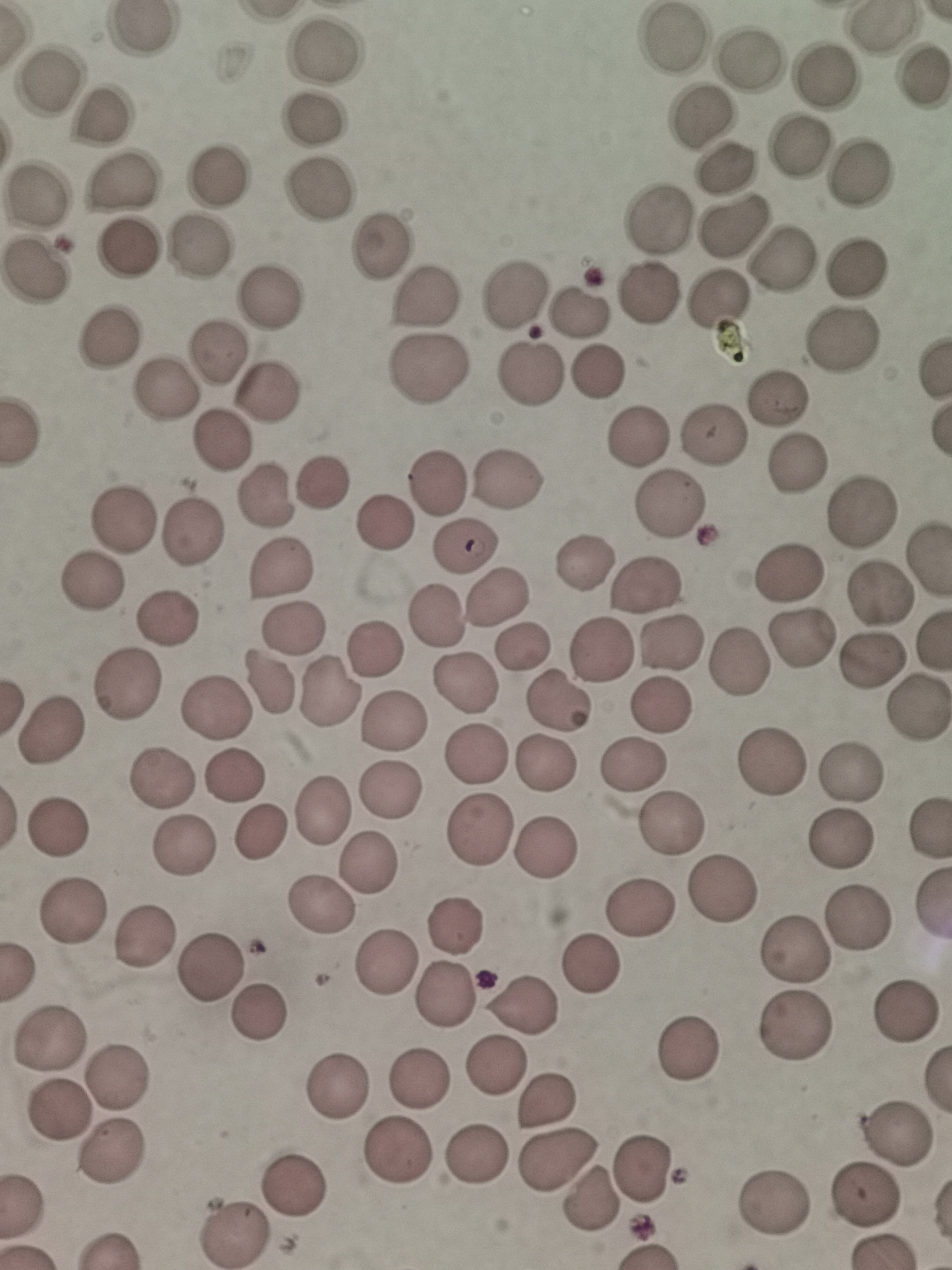

Approximate object centers, in pixels from the top-left corner.
Summary:
  - Cell locations: (x=671, y=41), (x=324, y=52), (x=752, y=59), (x=825, y=76), (x=918, y=76), (x=48, y=82), (x=99, y=114), (x=701, y=117), (x=313, y=123), (x=797, y=144), (x=727, y=167), (x=857, y=171), (x=216, y=174), (x=124, y=182), (x=319, y=194), (x=37, y=195), (x=655, y=220), (x=731, y=225), (x=380, y=246), (x=130, y=247), (x=200, y=248), (x=781, y=258), (x=856, y=267), (x=38, y=269), (x=517, y=294), (x=648, y=294), (x=423, y=296), (x=268, y=299), (x=721, y=301), (x=578, y=312), (x=108, y=336), (x=844, y=342), (x=217, y=352), (x=423, y=369), (x=597, y=372), (x=530, y=374), (x=166, y=391), (x=268, y=393), (x=776, y=400), (x=715, y=434), (x=638, y=437), (x=219, y=441), (x=797, y=463), (x=509, y=479), (x=438, y=481), (x=323, y=482), (x=266, y=497), (x=671, y=505), (x=862, y=510), (x=124, y=520), (x=387, y=521), (x=194, y=531), (x=466, y=546), (x=584, y=561), (x=277, y=568), (x=790, y=572), (x=90, y=582), (x=649, y=588), (x=496, y=594), (x=879, y=594), (x=432, y=617), (x=168, y=618), (x=294, y=630), (x=800, y=638), (x=670, y=640), (x=523, y=646), (x=375, y=649), (x=604, y=649), (x=872, y=657), (x=739, y=660), (x=269, y=683), (x=127, y=684), (x=462, y=684), (x=330, y=695), (x=556, y=700), (x=663, y=704), (x=915, y=706), (x=215, y=711), (x=392, y=720), (x=50, y=729), (x=477, y=755), (x=633, y=763), (x=547, y=764), (x=771, y=765), (x=233, y=774), (x=850, y=775), (x=162, y=778), (x=390, y=789), (x=324, y=810), (x=672, y=823), (x=59, y=827), (x=480, y=830), (x=258, y=835), (x=842, y=842), (x=548, y=846), (x=185, y=847), (x=370, y=861), (x=721, y=890), (x=318, y=908), (x=643, y=908), (x=70, y=914), (x=858, y=921), (x=457, y=925), (x=141, y=937), (x=798, y=945), (x=386, y=957), (x=592, y=963), (x=211, y=965), (x=444, y=996), (x=526, y=1004), (x=901, y=1013), (x=259, y=1014), (x=793, y=1026), (x=50, y=1036), (x=692, y=1046), (x=494, y=1067), (x=121, y=1075), (x=339, y=1080), (x=420, y=1082), (x=547, y=1101), (x=57, y=1115), (x=896, y=1133), (x=398, y=1152), (x=480, y=1155), (x=556, y=1155), (x=115, y=1156), (x=648, y=1165), (x=294, y=1183), (x=868, y=1197), (x=593, y=1200), (x=780, y=1200), (x=238, y=1236)
  - Image size: 952×1270 pixels
  - Stain: Giemsa
  - Field of view: single
  - Capture: smartphone camera at the microscope eyepiece
  - Preparation: thin smear